Assess this cell for malaria.
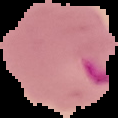

It is parasitized.

The area outside the segmented cell region is set to black. From a thin blood film. Image is 118×118 pixels.